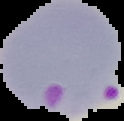

malaria_status: parasitized
preparation: thin blood smear
image_size: 124×121 pixels
image_type: cell region segmented out of the field of view; surrounding area masked to black